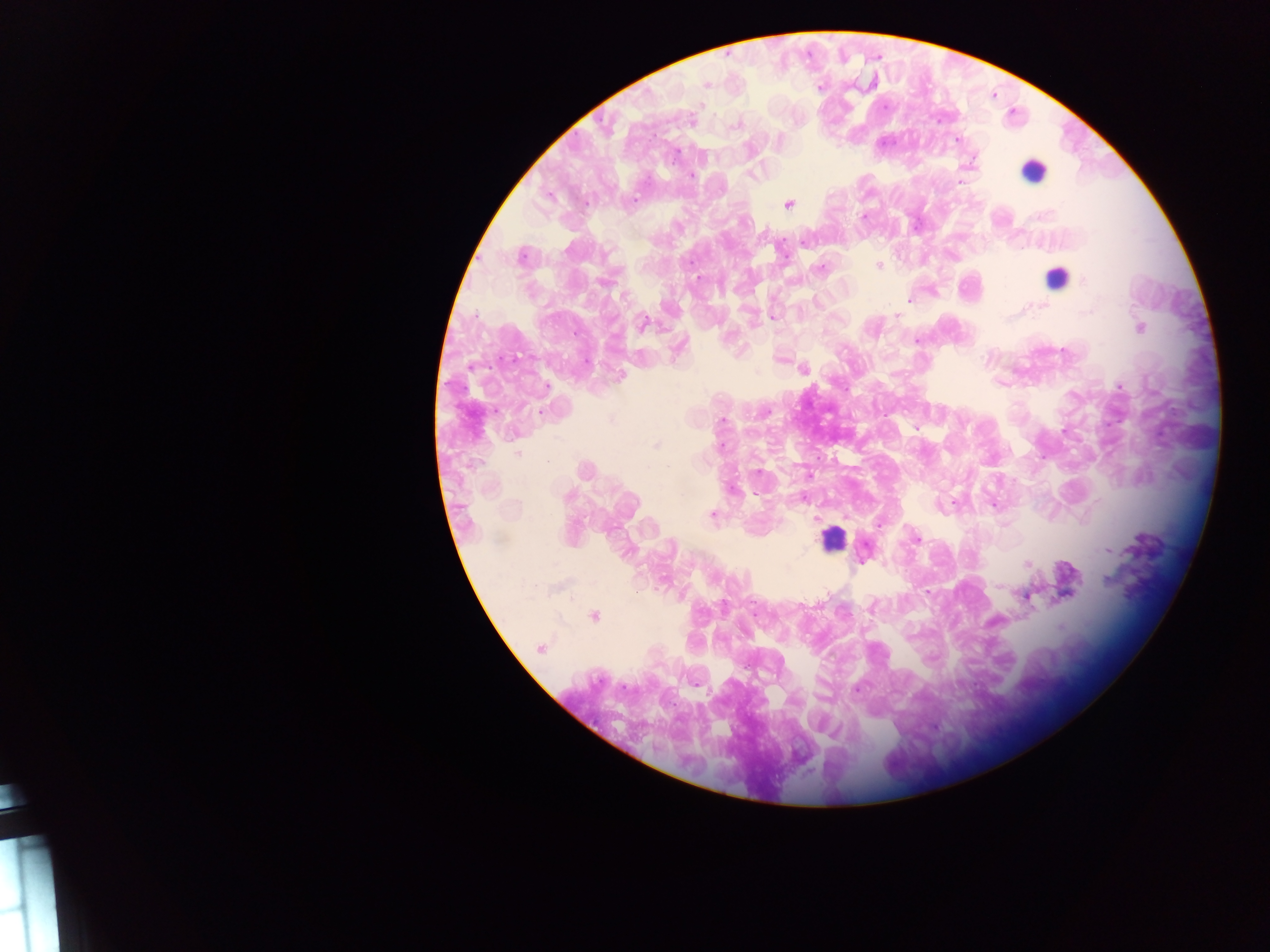
Plasmodium parasite locations = approximate centers as {x, y} in pixels: {706, 85}, {871, 85}, {820, 87}, {885, 107}, {691, 121}, {735, 125}, {957, 140}, {676, 155}, {752, 174}, {692, 175}, {960, 182}, {635, 199}, {789, 203}, {864, 217}, {805, 241}, {521, 256}, {878, 266}, {819, 269}, {698, 279}, {1085, 280}, {910, 300}, {1043, 306}, {896, 315}, {774, 317}, {643, 323}, {1140, 328}, {917, 340}, {586, 362}, {804, 369}, {621, 376}, {546, 387}, {1119, 387}, {541, 412}, {767, 412}, {722, 420}, {916, 429}, {655, 445}, {721, 446}, {517, 453}, {547, 460}, {585, 469}, {758, 472}, {732, 489}, {756, 495}, {568, 496}, {993, 505}, {712, 515}, {816, 518}, {878, 525}, {917, 539}, {1107, 551}, {1027, 565}, {1107, 580}, {998, 586}, {826, 592}, {927, 592}, {1064, 596}, {1027, 597}, {872, 608}, {594, 616}, {1060, 627}, {540, 648}, {856, 690}, {935, 727}
image size = 1270×952 pixels
preparation = thick blood smear
country = Ghana
capture = mobile-phone photograph through a microscope
leukocyte locations = approximate centers as {x, y} in pixels: {1033, 171}, {1056, 278}, {833, 538}
field of view = single